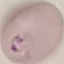
result = malaria parasites detected
preparation = thin blood film
stain = Giemsa
image type = cell patch, automatically extracted from a larger field of view and resized to 64 × 64 pixels
capture = smartphone camera at the microscope eyepiece